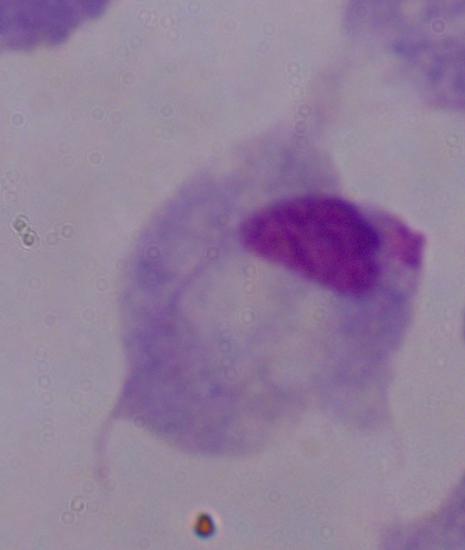
Captured at 1000x magnification. Micrograph. A trichomonad is shown.